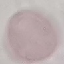

malaria status = uninfected
preparation = thin blood film
stain = Giemsa
capture = smartphone through the microscope eyepiece
image type = automatically extracted cell patch, resized to 64 × 64 pixels